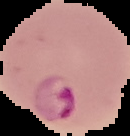
From a thin blood smear. Cell region segmented out of the field of view; the surrounding area is masked to black. Malaria status: parasitized. Image is 130×136 pixels.